Point out each leukocyte.
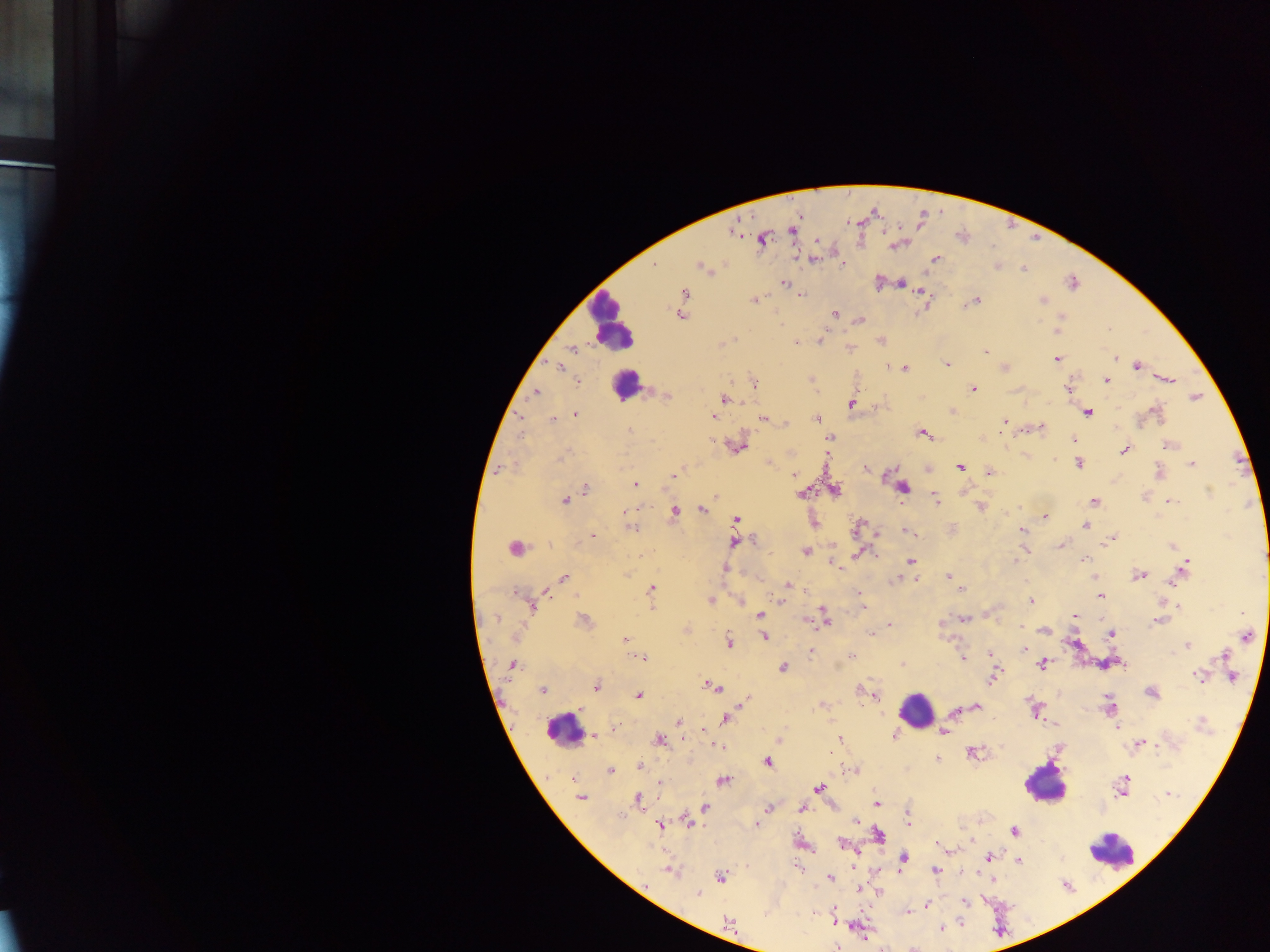
Approximate centers as x y in pixels.
Leukocytes: 610 322; 623 384; 916 709; 563 728; 1045 784; 1110 851.

{
  "field_of_view": "single",
  "country": "Ghana",
  "image_size": "1270×952 pixels",
  "preparation": "thick blood film",
  "plasmodium_parasite_locations": "approximate centers as x y in pixels: 734 231; 792 231; 762 239; 899 244; 814 258; 935 259; 843 264; 653 266; 701 266; 997 266; 1024 268; 784 283; 877 283; 901 283; 1072 283; 920 291; 683 294; 800 295; 755 299; 1042 300; 975 301; 968 303; 681 313; 834 314; 1061 316; 859 320; 1056 329; 820 340; 881 340; 721 343; 796 343; 849 348; 572 349; 986 352; 1056 358; 1114 358; 945 364; 1136 365; 560 366; 1004 367; 904 368; 1106 379; 811 380; 1167 380; 577 382; 754 384; 972 389; 1068 389; 535 393; 666 394; 1195 397; 725 399; 852 402; 953 410; 1086 411; 1156 412; 575 414; 713 416; 818 418; 552 419; 764 419; 1004 422; 1042 426; 1025 430; 630 432; 922 433; 830 438; 980 438; 1073 440; 735 445; 1169 445; 1124 450; 767 463; 1078 463; 1191 463; 960 466; 499 469; 866 469; 926 469; 678 470; 988 472; 1159 472; 674 473; 794 474; 635 485; 902 487; 585 489; 834 489; 963 490; 802 494; 715 496; 936 499; 565 500; 1169 501; 1094 502; 980 507; 1019 507; 627 508; 702 509; 674 510; 1045 518; 736 520; 812 521; 1085 525; 858 526; 631 527; 951 529; 1021 529; 908 532; 877 534; 591 535; 1112 537; 734 542; 1061 545; 1171 546; 514 548; 1025 549; 804 551; 858 553; 1083 559; 832 561; 911 561; 724 568; 1183 568; 1139 575; 949 576; 1094 576; 564 577; 897 578; 788 585; 962 589; 650 590; 540 591; 858 593; 1098 596; 740 599; 709 600; 781 601; 1031 601; 532 604; 862 607; 1179 607; 991 613; 1241 613; 824 614; 759 615; 1074 616; 963 619; 806 620; 1158 620; 584 621; 825 622; 941 624; 889 625; 1021 626; 685 629; 1044 630; 870 632; 1110 633; 1247 636; 764 637; 624 640; 728 642; 1074 642; 1187 645; 1025 649; 811 650; 989 653; 1224 654; 852 656; 637 657; 644 657; 963 658; 1122 663; 902 664; 1042 664; 510 665; 782 667; 1199 675; 1232 677; 991 678; 595 685; 711 685; 542 689; 860 690; 871 692; 1151 692; 876 695; 638 696; 745 699; 821 704; 1109 705; 976 706; 1034 709; 954 711; 725 719; 678 723; 1202 723; 1055 725; 1117 726; 615 728; 943 732; 893 734; 594 735; 659 740; 838 740; 779 741; 1138 744; 719 745; 972 752; 937 758; 766 761; 639 766; 611 770; 855 770; 722 780; 660 782; 1123 785; 818 788; 1169 793; 580 797; 637 799; 876 804; 704 807; 801 808; 768 809; 907 813; 762 814; 856 820; 687 821; 907 821; 756 823; 660 825; 1013 831; 878 835; 970 840; 843 843; 948 850; 988 857; 902 860; 1018 860; 853 866; 799 868; 669 870; 934 870; 720 876; 992 877; 829 879; 861 890; 877 892; 697 894; 964 901; 926 906; 906 910; 835 921; 728 922; 941 928",
  "capture": "mobile-phone photograph through a microscope"
}